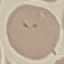

Summary:
  - Result: malaria parasites identified
  - Stain: Giemsa
  - Preparation: thin blood film
  - Image type: cell patch, automatically extracted from a larger field of view and resized to 64 × 64 pixels
  - Capture: smartphone camera at the microscope eyepiece